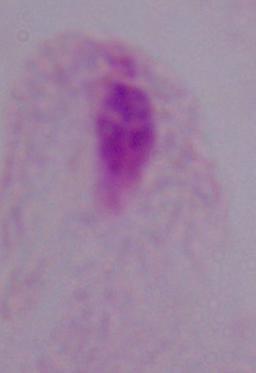
Captured at 1000x magnification. Photomicrograph. A trichomonad is seen.